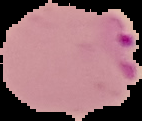
Cell region segmented out of the field of view; the surrounding area is masked to black. Malaria status: parasitized. From a thin blood film. Image is 142×121 pixels.